Assess this cell for malaria.
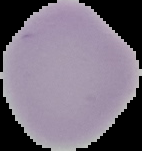

Uninfected.

Summary:
  - Image type: cell region segmented out of the field of view; surrounding area masked to black
  - Image size: 142×151 pixels
  - Preparation: thin blood film